Report the malaria status of this cell.
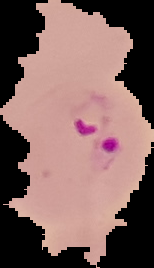
Parasitized.

Summary:
  - Image type: cell region segmented out of the field of view; surrounding area masked to black
  - Image size: 154×268 pixels
  - Preparation: thin blood smear